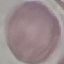

malaria status = uninfected
capture = smartphone camera at the microscope eyepiece
image type = automatically extracted cell patch, resized to 64 × 64 pixels
preparation = thin blood film
stain = Giemsa